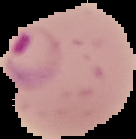 Malaria status: parasitized. From a thin blood smear. Segmented cell region on a black background. Image is 136×139 pixels.